Assess the morphology of the erythrocytes.
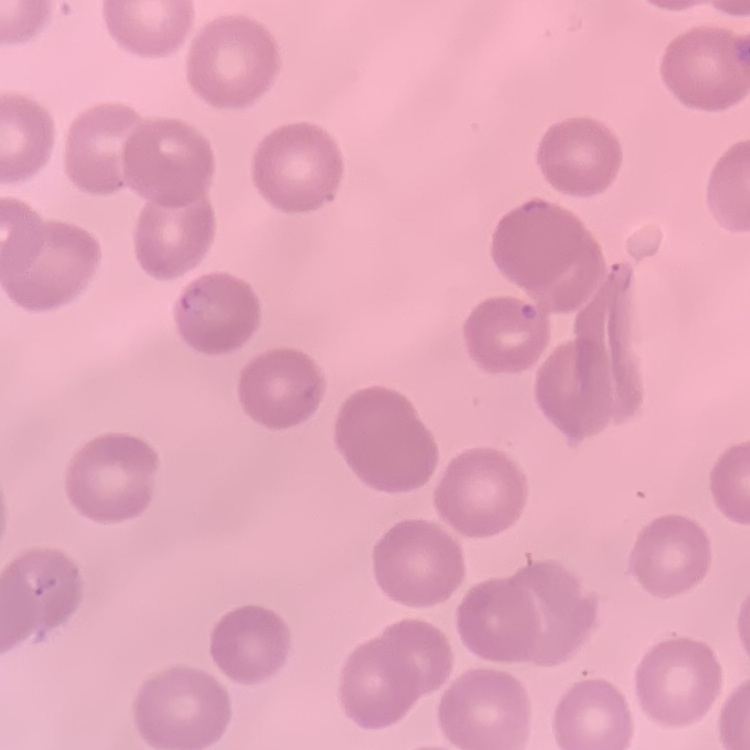

No rouleaux formation.

{
  "image_type": "square crop of a larger photomicrograph",
  "stain": "Field's or Giemsa",
  "preparation": "thin peripheral smear"
}